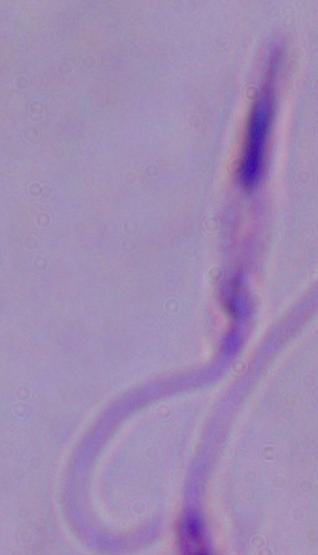
Summary:
  - Magnification: 1000x
  - Identification: Leishmania
  - Modality: micrograph